Identify the blood parasite species.
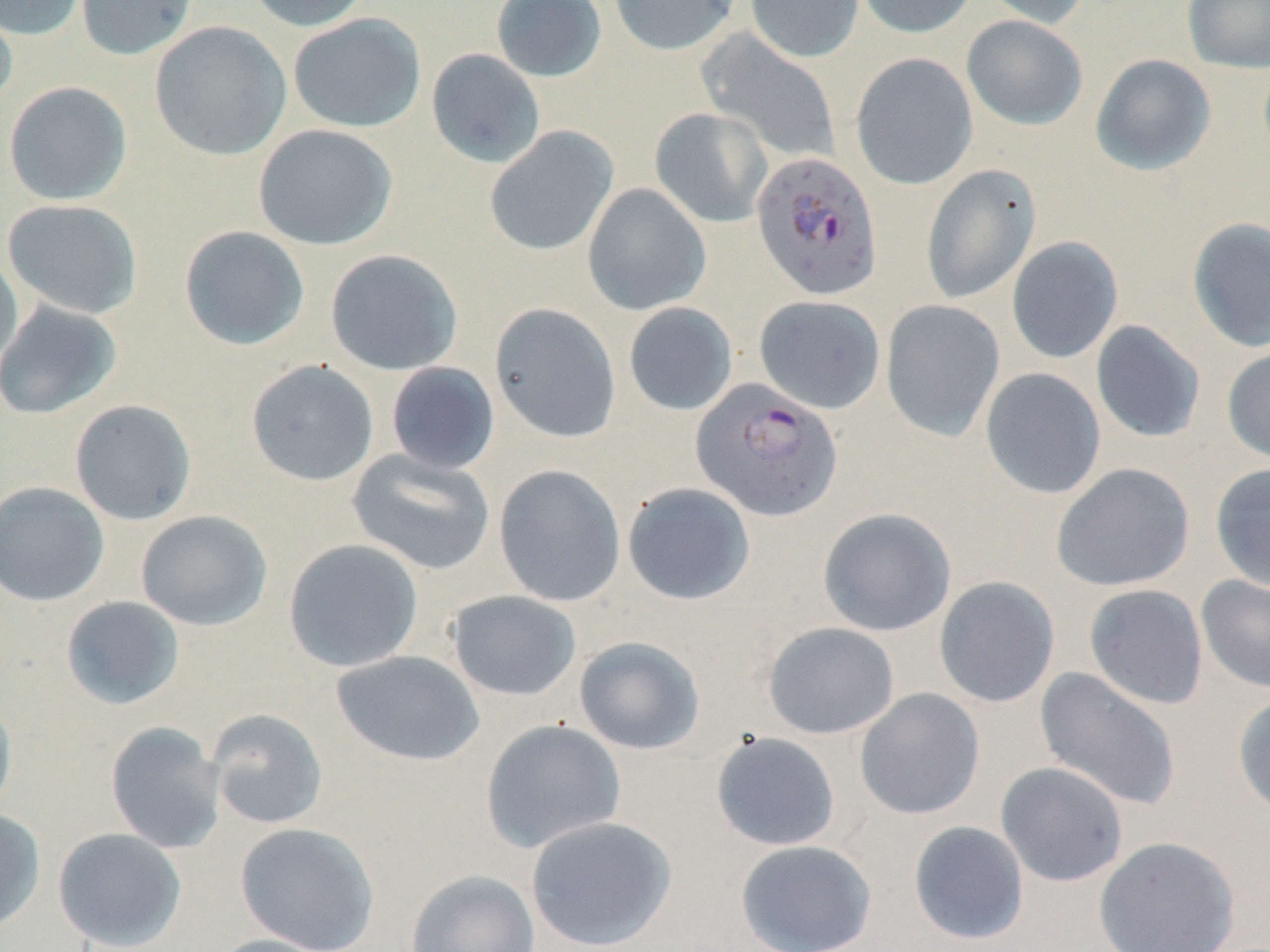
Plasmodium falciparum.

Summary:
  - Coordinate format: approximate bounding boxes as [x1, y1, x2, y2] in pixels
  - Uninfected red blood cell locations: [0, 0, 88, 41], [75, 0, 197, 61], [245, 0, 373, 32], [491, 0, 607, 83], [609, 0, 741, 56], [745, 0, 864, 63], [852, 0, 977, 38], [980, 0, 1091, 29], [1182, 0, 1270, 73], [0, 5, 19, 114], [288, 13, 426, 133], [961, 15, 1088, 130], [149, 21, 292, 161], [698, 30, 841, 163], [426, 49, 546, 168], [851, 53, 978, 190], [1090, 53, 1216, 176], [3, 81, 132, 205], [650, 107, 773, 228], [253, 124, 397, 250], [485, 126, 618, 256], [921, 164, 1041, 304], [582, 183, 711, 316], [3, 198, 143, 320], [1187, 218, 1270, 352], [179, 225, 310, 351], [1006, 236, 1124, 364], [0, 249, 23, 379], [325, 249, 463, 376], [754, 295, 886, 414], [880, 299, 1005, 442], [0, 301, 122, 420], [623, 302, 738, 416], [490, 303, 621, 443], [1091, 320, 1206, 443], [1221, 344, 1270, 466], [246, 359, 380, 487], [385, 361, 500, 475], [980, 367, 1106, 500], [69, 399, 197, 525], [346, 449, 496, 576], [1051, 462, 1195, 592], [1209, 463, 1270, 592], [493, 464, 626, 608], [0, 481, 110, 607], [622, 482, 756, 605], [817, 507, 957, 637], [135, 510, 272, 631], [283, 538, 424, 673], [1196, 575, 1270, 694], [934, 576, 1060, 708], [1083, 583, 1208, 709], [446, 590, 582, 701], [60, 596, 185, 711], [762, 622, 899, 740], [573, 636, 706, 755], [331, 650, 485, 767], [1035, 667, 1182, 811], [854, 688, 985, 820], [1232, 690, 1270, 819], [0, 691, 17, 819], [206, 708, 329, 830], [480, 719, 627, 854], [105, 722, 227, 854], [710, 731, 841, 851], [995, 761, 1129, 887], [0, 807, 46, 935], [525, 815, 678, 952], [908, 820, 1029, 945], [235, 822, 380, 951], [52, 827, 188, 951], [1093, 836, 1240, 952], [734, 839, 878, 952], [405, 869, 541, 952], [205, 933, 342, 952]
  - Plasmodium falciparum-infected red blood cell locations: [751, 150, 883, 301], [691, 379, 842, 522]
  - Stain: May-Grünwald-Giemsa
  - Modality: light microscopy
  - Preparation: thin blood film
  - Image size: 1270×952 pixels
  - Field of view: one of a larger specimen
  - Magnification: 1000x